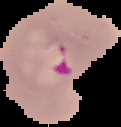

{
  "result": "Plasmodium parasites detected",
  "image_type": "cell region segmented out of the field of view; surrounding area masked to black",
  "image_size": "121×127 pixels",
  "preparation": "thin blood smear"
}